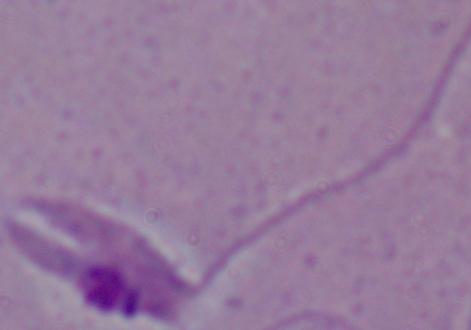
modality = photomicrograph
identification = Leishmania
magnification = 1000x